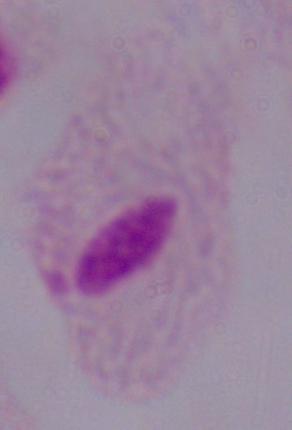

Micrograph. 1000x magnification. A trichomonad is shown.